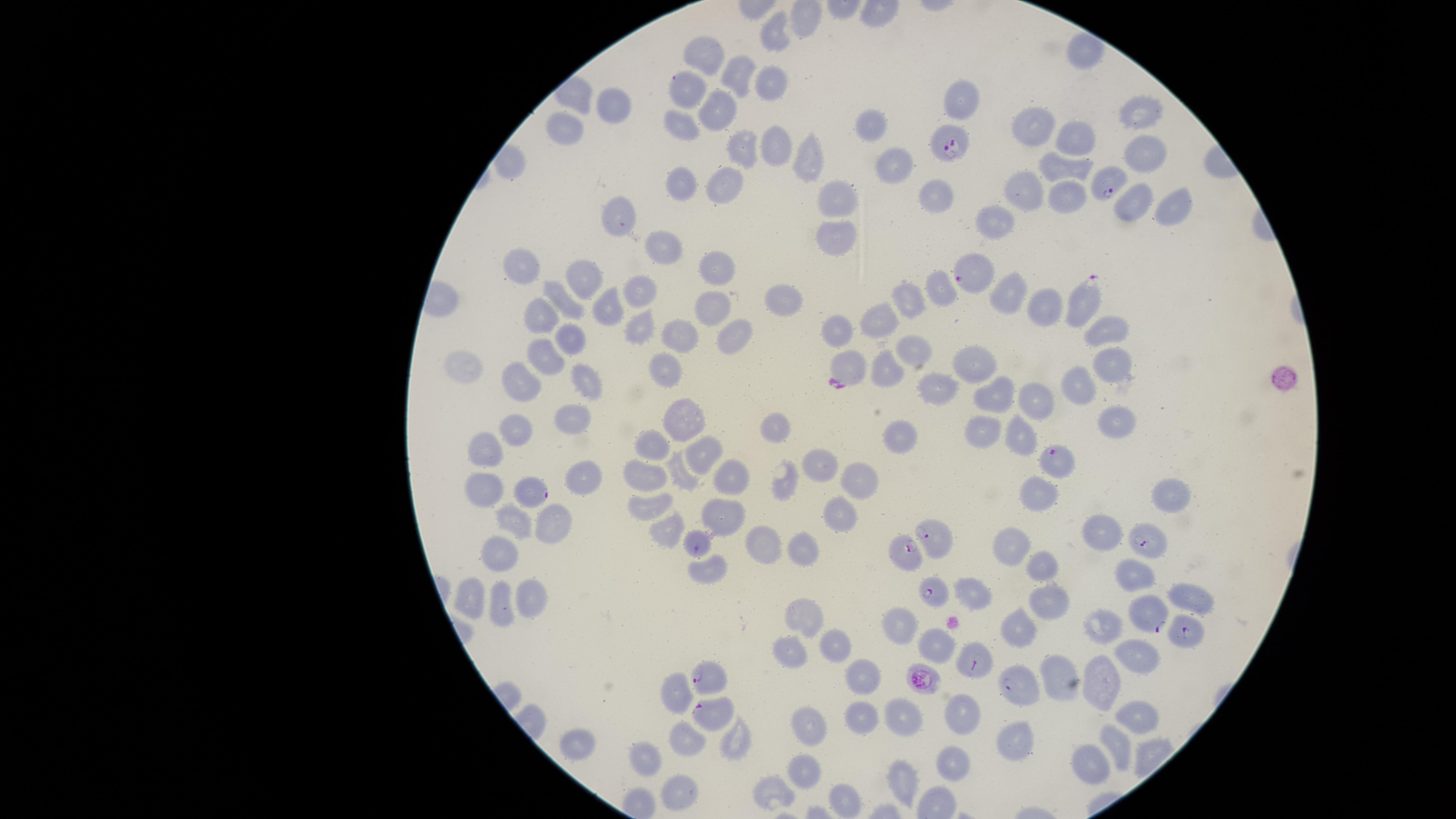
{
  "image_size": "1456×819 pixels",
  "uninfected_red_blood_cells": "approximate marker points as {x, y} in pixels: {776, 32}, {706, 53}, {738, 69}, {769, 78}, {688, 85}, {618, 101}, {719, 105}, {1142, 112}, {684, 120}, {1038, 123}, {873, 124}, {566, 126}, {1077, 134}, {745, 144}, {780, 144}, {1142, 156}, {810, 161}, {893, 162}, {1066, 167}, {683, 182}, {731, 186}, {1029, 186}, {939, 190}, {837, 194}, {1064, 199}, {1131, 199}, {1177, 200}, {622, 218}, {997, 226}, {842, 229}, {661, 246}, {523, 261}, {718, 266}, {637, 285}, {581, 287}, {939, 287}, {1011, 294}, {561, 300}, {909, 301}, {781, 302}, {1041, 302}, {608, 303}, {716, 308}, {540, 311}, {882, 317}, {640, 320}, {1111, 321}, {838, 325}, {736, 332}, {681, 333}, {575, 336}, {915, 353}, {974, 355}, {547, 356}, {848, 359}, {1114, 363}, {886, 366}, {662, 367}, {467, 368}, {588, 376}, {522, 381}, {935, 382}, {1078, 387}, {1000, 391}, {1041, 394}, {689, 417}, {575, 419}, {1117, 420}, {520, 425}, {779, 426}, {981, 428}, {1015, 433}, {906, 440}, {652, 449}, {492, 455}, {705, 458}, {826, 465}, {684, 473}, {642, 475}, {858, 475}, {735, 477}, {586, 481}, {785, 481}, {487, 488}, {1038, 490}, {1171, 490}, {648, 503}, {721, 510}, {837, 511}, {513, 521}, {552, 523}, {1106, 532}, {663, 534}, {759, 540}, {802, 545}, {699, 547}, {1015, 547}, {500, 557}, {1042, 565}, {707, 573}, {1134, 576}, {469, 592}, {978, 595}, {1192, 598}, {527, 599}, {1046, 603}, {502, 604}, {805, 615}, {903, 624}, {1108, 625}, {1014, 630}, {935, 645}, {835, 647}, {1135, 652}, {787, 653}, {865, 679}, {1069, 681}, {1102, 681}, {680, 688}, {959, 712}, {1136, 714}, {865, 716}, {904, 716}, {811, 725}, {737, 735}, {688, 738}, {1018, 738}, {581, 741}, {1121, 744}, {650, 758}, {1093, 762}, {954, 763}, {804, 768}, {900, 782}, {676, 790}, {774, 790}, {842, 798}",
  "species": "Plasmodium falciparum",
  "presence": "malaria parasites seen",
  "parasitized_red_blood_cells": "approximate marker points as {x, y} in pixels: {952, 146}, {1109, 187}, {980, 291}, {1085, 302}, {1058, 457}, {535, 488}, {935, 534}, {1146, 540}, {902, 552}, {937, 594}, {1146, 613}, {1182, 629}, {973, 664}, {922, 677}, {712, 681}, {1012, 686}, {711, 712}",
  "field_of_view": "single",
  "capture": "smartphone photograph through the microscope eyepiece",
  "visible_region": "circular",
  "stain": "Giemsa",
  "preparation": "thin smear of blood"
}